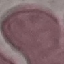

Summary:
  - Result: negative for malaria parasites
  - Preparation: thin blood smear
  - Capture: smartphone through the microscope eyepiece
  - Stain: Giemsa
  - Image type: cell patch, automatically extracted from a larger field of view and resized to 64 × 64 pixels